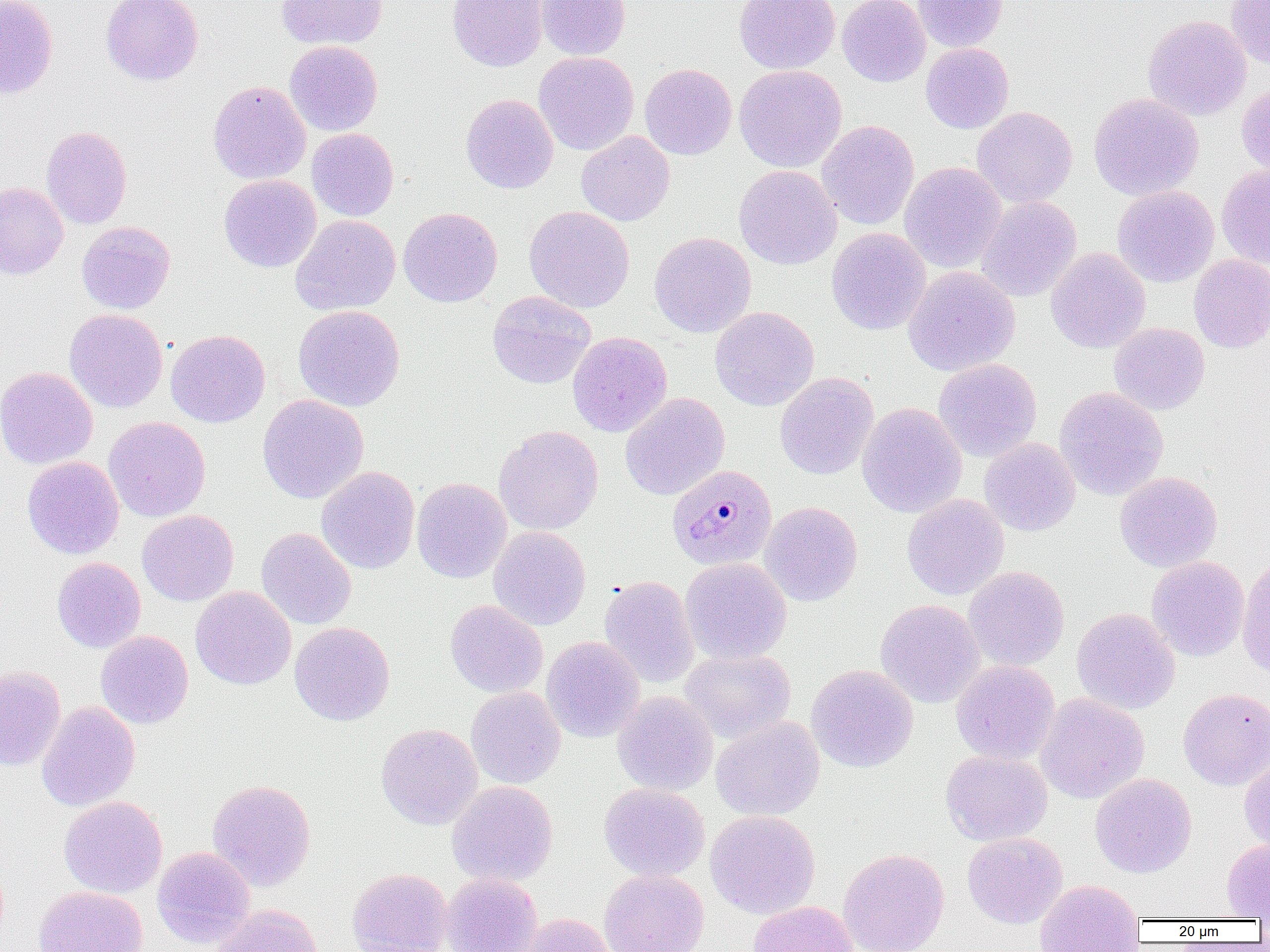
Summary:
  - Coordinate format: approximate bounding boxes as (x1,y1)-(x2,y2) corner pairs in pixels
  - Plasmodium malariae-infected red blood cell locations: (667,464)-(777,570)
  - Uninfected red blood cell locations: (0,0)-(58,99), (101,0)-(203,86), (276,0)-(387,49), (447,0)-(547,72), (534,0)-(631,60), (734,0)-(840,74), (837,0)-(930,87), (913,0)-(1007,52), (1226,0)-(1270,68), (1143,15)-(1252,121), (284,41)-(383,136), (921,43)-(1014,134), (534,51)-(639,156), (640,63)-(737,160), (734,65)-(847,172), (1236,79)-(1270,178), (208,80)-(311,184), (1088,92)-(1204,200), (461,93)-(559,193), (972,106)-(1077,208), (816,120)-(919,230), (41,125)-(132,229), (306,128)-(399,221), (576,131)-(675,226), (899,162)-(1006,273), (1216,163)-(1270,268), (734,165)-(842,270), (219,174)-(321,272), (0,182)-(68,280), (1112,185)-(1219,287), (976,196)-(1082,302), (524,205)-(635,313), (398,206)-(502,307), (290,215)-(401,316), (76,221)-(176,314), (827,227)-(931,335), (649,231)-(756,338), (1046,247)-(1150,354), (1188,255)-(1270,352), (903,266)-(1020,376), (487,290)-(596,389), (293,305)-(405,411), (710,306)-(819,410), (64,308)-(167,413), (1109,322)-(1209,415), (165,329)-(270,427), (567,331)-(672,437), (933,358)-(1042,462), (0,366)-(98,469), (775,373)-(878,480), (1054,387)-(1169,500), (620,392)-(730,500), (257,394)-(369,503), (857,403)-(967,518), (103,416)-(211,522), (494,425)-(604,535), (979,437)-(1080,536), (22,456)-(124,559), (316,467)-(419,574), (1114,471)-(1222,572), (412,477)-(512,583), (901,494)-(1009,600), (760,502)-(863,607), (137,510)-(238,606), (488,526)-(590,630), (256,527)-(356,630), (1146,556)-(1249,662), (1237,556)-(1270,680), (51,557)-(146,653), (680,558)-(792,664), (963,566)-(1070,671), (599,575)-(699,689), (190,586)-(296,689), (875,599)-(985,708), (445,600)-(547,697), (1072,607)-(1180,715), (289,621)-(395,726), (96,630)-(194,729), (541,636)-(645,743), (679,648)-(795,742), (951,660)-(1060,765), (806,664)-(918,773), (0,665)-(66,771), (465,686)-(566,790), (1178,687)-(1270,790), (612,691)-(718,796), (1035,692)-(1149,804), (36,700)-(140,811), (711,716)-(825,821), (376,723)-(483,830), (941,750)-(1053,846), (1239,754)-(1270,855), (1090,773)-(1197,878), (207,779)-(316,891), (447,781)-(558,887), (599,783)-(710,882), (59,796)-(167,898), (705,810)-(821,919), (962,832)-(1067,929), (1221,838)-(1270,919), (152,846)-(255,948), (838,848)-(950,952), (347,867)-(453,952), (599,869)-(709,952), (441,872)-(543,952), (1035,879)-(1145,951), (33,886)-(147,952), (748,900)-(859,952), (211,904)-(323,952), (519,912)-(618,952)
  - Slide-level diagnosis: Plasmodium malariae
  - Magnification: 1000x
  - Preparation: thin blood film
  - Modality: light microscopy
  - Field of view: single
  - Image size: 1270×952 pixels